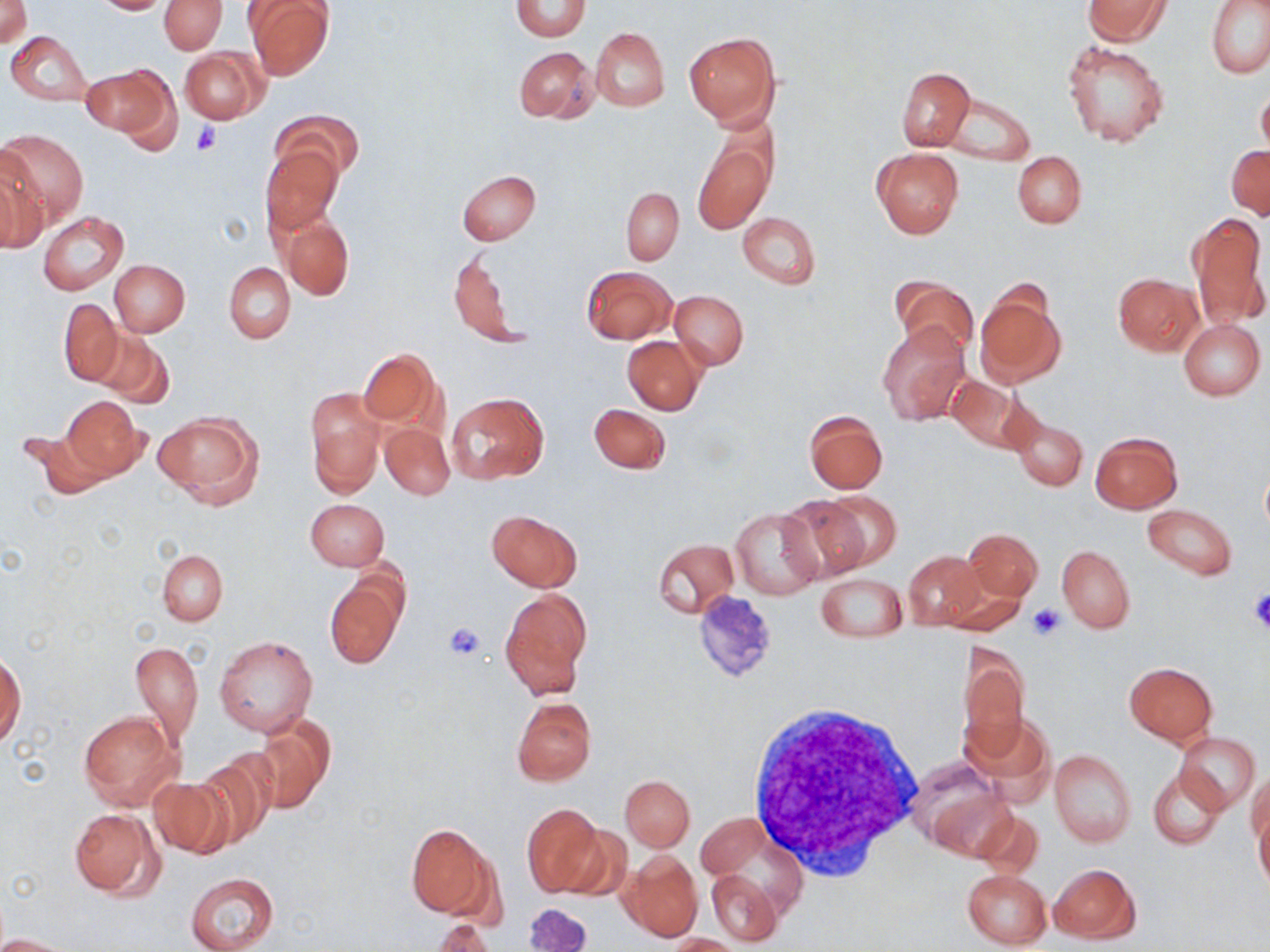

Summary:
  - Coordinate format: approximate bounding boxes as (x1,y1)-(x2,y2) corner pairs in pixels
  - Platelet locations: (190,123)-(221,156), (1247,586)-(1270,633), (1026,604)-(1067,640), (443,620)-(487,661)
  - White blood cell locations: (747,699)-(926,876)
  - Uninfected red blood cell locations: (0,0)-(31,48), (90,0)-(174,14), (1082,0)-(1170,45), (160,1)-(227,54), (244,1)-(334,81), (1207,1)-(1270,79), (511,2)-(590,40), (591,27)-(670,111), (5,31)-(90,105), (684,32)-(780,128), (1061,40)-(1170,148), (513,47)-(599,123), (180,48)-(266,123), (82,65)-(174,138), (897,68)-(974,150), (1256,87)-(1270,157), (941,94)-(1035,165), (270,110)-(362,183), (2,128)-(88,224), (692,142)-(774,235), (261,146)-(342,235), (1227,146)-(1269,220), (871,148)-(963,238), (0,150)-(44,252), (1013,151)-(1086,229), (457,170)-(541,245), (621,187)-(683,264), (38,211)-(129,295), (738,212)-(822,289), (1186,213)-(1269,327), (282,215)-(353,301), (448,249)-(533,349), (110,260)-(190,336), (103,263)-(181,407), (225,263)-(295,344), (581,265)-(675,344), (1113,274)-(1203,356), (892,276)-(979,356), (975,286)-(1065,388), (669,290)-(749,369), (57,298)-(124,386), (642,304)-(740,399), (1178,318)-(1266,400), (878,323)-(970,425), (88,330)-(173,407), (621,337)-(707,416), (358,347)-(442,431), (946,373)-(1032,455), (305,389)-(385,498), (447,392)-(548,485), (61,396)-(145,481), (589,403)-(672,474), (804,411)-(887,493), (157,412)-(262,507), (1011,414)-(1087,492), (380,422)-(455,500), (16,426)-(112,501), (1089,431)-(1183,513), (1259,461)-(1270,544), (792,492)-(899,579), (305,498)-(390,571), (1141,503)-(1238,579), (730,507)-(824,600), (486,510)-(582,591), (965,528)-(1043,602), (653,538)-(740,618), (1057,545)-(1134,633), (157,549)-(227,626), (902,552)-(986,629), (816,572)-(908,643), (325,576)-(406,670), (499,589)-(591,699), (213,635)-(318,737), (129,640)-(202,749), (957,651)-(1029,755), (0,653)-(25,752), (1124,662)-(1218,745), (510,696)-(598,786), (78,712)-(181,809), (965,712)-(1055,801), (253,716)-(335,809), (1175,732)-(1261,811), (191,749)-(278,848), (1049,749)-(1137,848), (914,764)-(1015,857), (1148,766)-(1228,851), (1247,769)-(1269,858), (620,776)-(695,851), (148,777)-(232,859), (520,803)-(604,896), (68,807)-(163,899), (1254,810)-(1270,896), (972,811)-(1043,878), (549,823)-(631,901), (407,824)-(493,916), (617,850)-(704,942), (1049,863)-(1141,944), (960,868)-(1051,949), (707,869)-(781,946), (184,872)-(279,952), (433,921)-(497,952), (0,932)-(75,952), (665,933)-(741,952)
  - Slide-level diagnosis: no evidence of blood parasites
  - Stain: May-Grünwald-Giemsa
  - Field of view: single
  - Modality: light microscopy
  - Magnification: 1000x
  - Preparation: thin blood film
  - Image size: 1270×952 pixels